Comment on the morphology of the red blood cells.
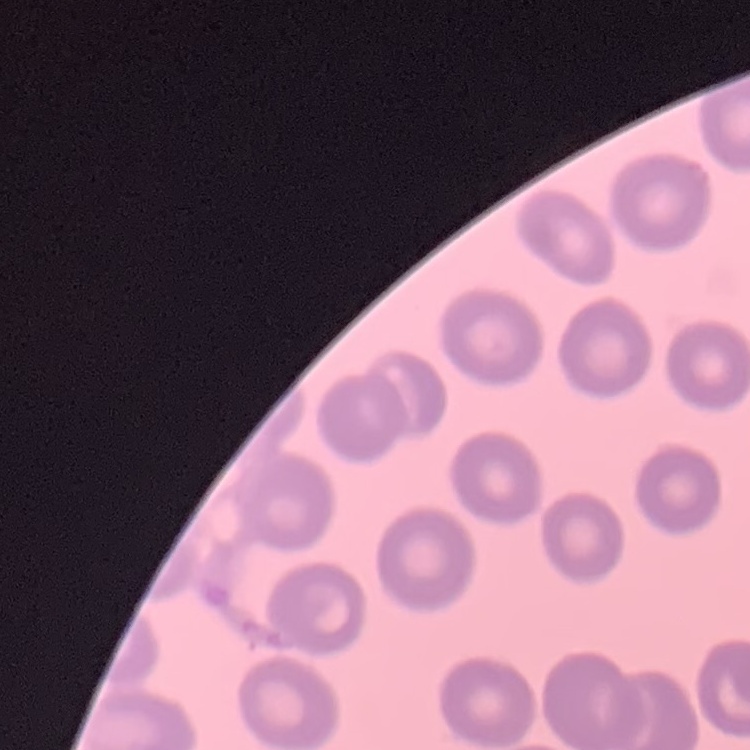
They show no rouleaux formation.

image type = square crop of a larger photomicrograph
stain = Field's or Giemsa
preparation = thin peripheral smear